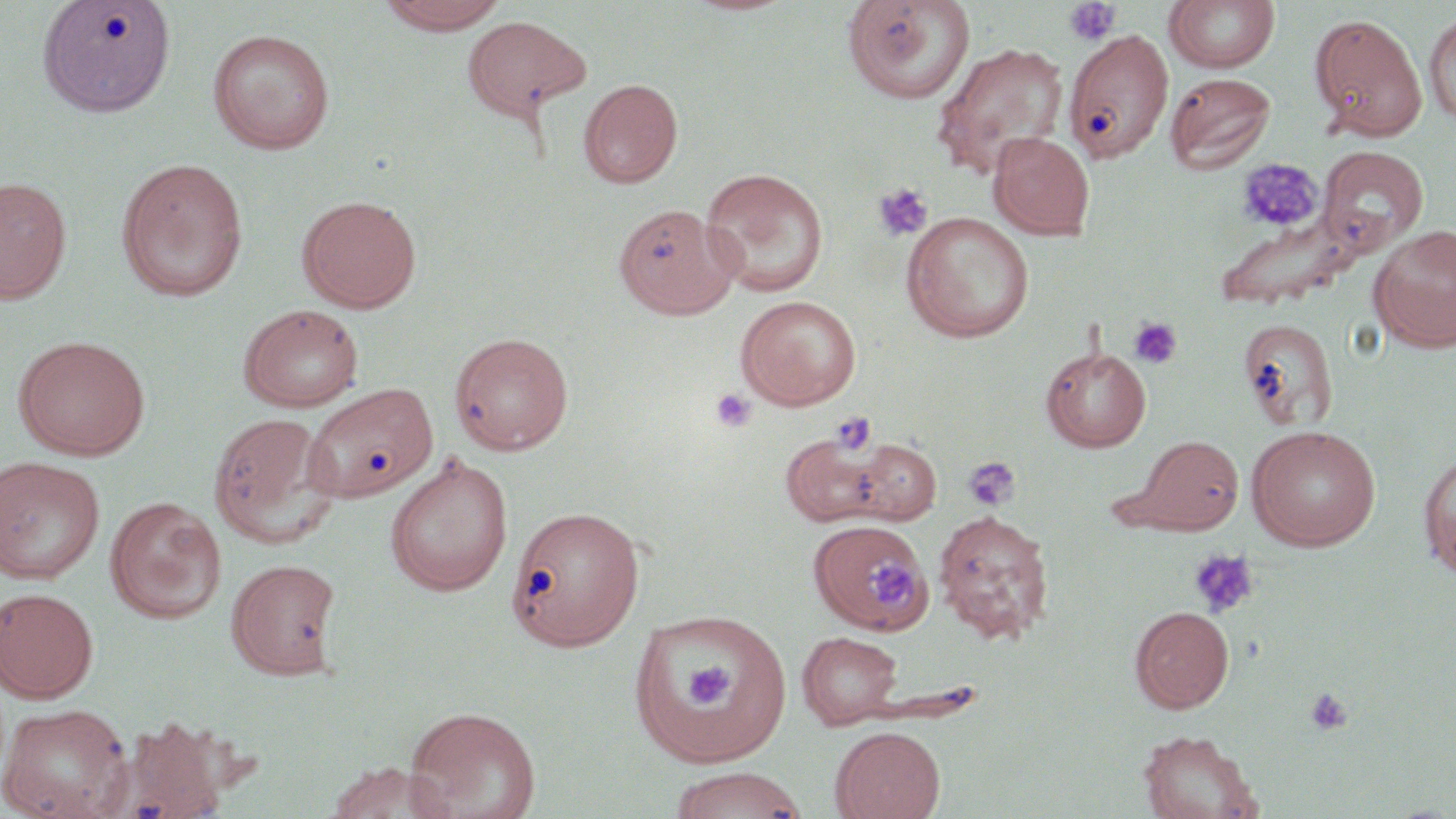

slide-level diagnosis = negative for blood parasites
uninfected red blood cell locations = approximate bounding boxes as [x1, y1, x2, y2] in pixels: [37, 0, 176, 118], [374, 0, 509, 34], [682, 0, 798, 17], [841, 0, 976, 106], [1164, 1, 1280, 74], [1424, 8, 1456, 127], [1309, 13, 1427, 140], [461, 15, 590, 121], [207, 28, 335, 154], [1064, 29, 1174, 163], [932, 42, 1070, 179], [1165, 72, 1277, 175], [578, 79, 682, 188], [989, 131, 1095, 241], [1317, 146, 1429, 257], [115, 157, 249, 303], [700, 167, 829, 298], [0, 176, 72, 304], [297, 194, 422, 313], [613, 203, 740, 319], [1213, 206, 1363, 313], [900, 211, 1035, 343], [1368, 224, 1456, 352], [735, 294, 862, 409], [238, 303, 365, 413], [1238, 318, 1339, 433], [450, 331, 574, 455], [12, 335, 151, 460], [1040, 344, 1152, 452], [303, 382, 439, 504], [207, 412, 340, 548], [1246, 424, 1381, 551], [779, 433, 893, 528], [1132, 435, 1245, 534], [847, 437, 942, 525], [1418, 450, 1455, 577], [384, 452, 513, 597], [0, 456, 105, 584], [105, 496, 226, 624], [506, 504, 646, 651], [933, 509, 1055, 644], [815, 529, 939, 639], [225, 558, 342, 679], [0, 587, 99, 702], [1130, 605, 1234, 712], [628, 608, 792, 769], [797, 631, 904, 729], [0, 703, 133, 819], [404, 706, 541, 819], [105, 718, 235, 819], [830, 725, 945, 819], [1138, 729, 1261, 819], [324, 761, 456, 819], [666, 767, 809, 819]
magnification = 1000x
field of view = one of a larger specimen
modality = optical microscopy
image size = 1456×819 pixels
stain = May-Grünwald-Giemsa
preparation = thin blood film
platelet locations = approximate bounding boxes as [x1, y1, x2, y2] in pixels: [1063, 0, 1122, 47], [1237, 159, 1323, 232], [871, 182, 933, 242], [1128, 316, 1183, 369], [710, 387, 757, 434], [829, 411, 877, 455], [962, 455, 1022, 513], [1188, 548, 1258, 618], [866, 559, 918, 613], [682, 658, 739, 713], [1304, 688, 1353, 735]